Describe the morphology of the red blood cells.
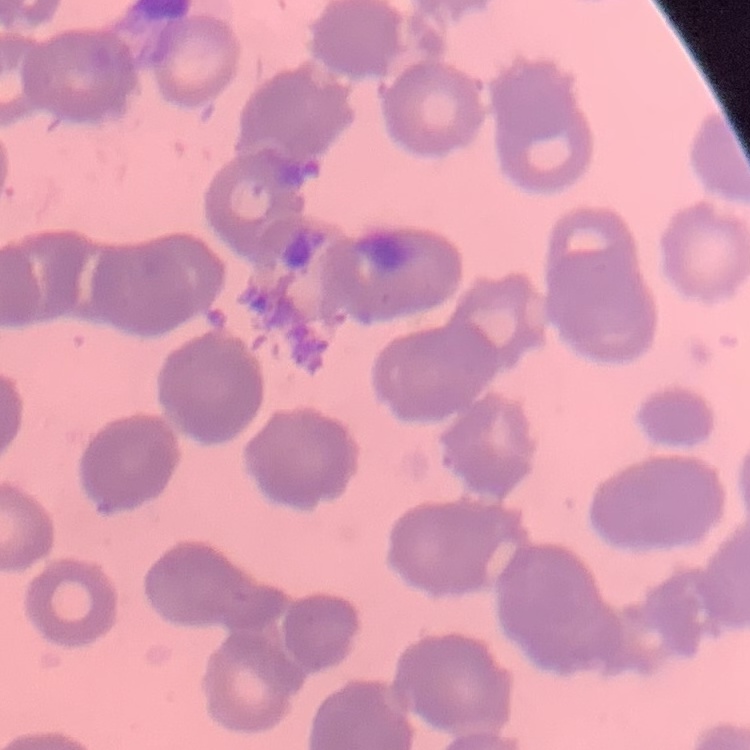
Rouleaux formation.

Stained with either Field's or Giemsa. Thin blood smear. Square crop of a larger photomicrograph.